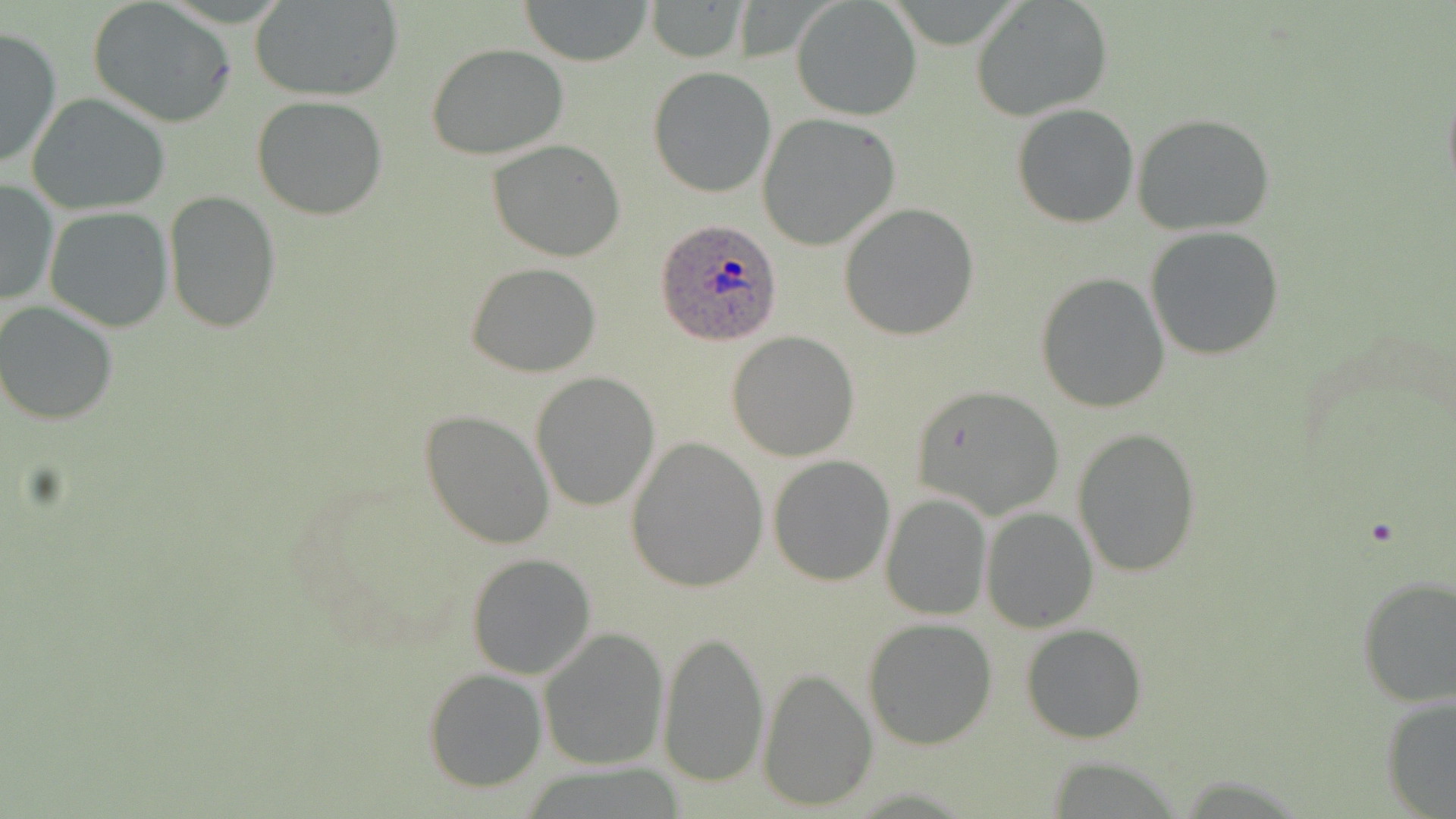
Approximate bounding boxes as named x1/y1/x2/y2 corners in pixels. Uninfected red blood cell locations: (x1=518, y1=0, x2=656, y2=66), (x1=250, y1=1, x2=404, y2=101), (x1=645, y1=1, x2=754, y2=64), (x1=794, y1=1, x2=921, y2=122), (x1=971, y1=2, x2=1113, y2=121), (x1=87, y1=4, x2=235, y2=127), (x1=0, y1=26, x2=62, y2=171), (x1=426, y1=44, x2=570, y2=162), (x1=648, y1=67, x2=777, y2=197), (x1=1441, y1=76, x2=1456, y2=201), (x1=27, y1=92, x2=171, y2=214), (x1=250, y1=96, x2=389, y2=221), (x1=1012, y1=103, x2=1140, y2=228), (x1=757, y1=113, x2=901, y2=250), (x1=1131, y1=113, x2=1275, y2=236), (x1=488, y1=139, x2=627, y2=261), (x1=1, y1=178, x2=58, y2=307), (x1=163, y1=190, x2=281, y2=333), (x1=838, y1=202, x2=981, y2=341), (x1=44, y1=206, x2=174, y2=332), (x1=1146, y1=226, x2=1284, y2=361), (x1=465, y1=261, x2=601, y2=378), (x1=1035, y1=272, x2=1171, y2=412), (x1=0, y1=302, x2=120, y2=424), (x1=726, y1=331, x2=859, y2=461), (x1=530, y1=371, x2=659, y2=511), (x1=908, y1=384, x2=1064, y2=520), (x1=420, y1=411, x2=554, y2=550), (x1=1073, y1=428, x2=1202, y2=579), (x1=626, y1=436, x2=769, y2=593), (x1=767, y1=455, x2=895, y2=587), (x1=880, y1=492, x2=992, y2=622), (x1=980, y1=506, x2=1096, y2=632), (x1=467, y1=552, x2=597, y2=680), (x1=1356, y1=576, x2=1455, y2=706), (x1=862, y1=618, x2=997, y2=749), (x1=1021, y1=624, x2=1148, y2=743), (x1=537, y1=626, x2=669, y2=772), (x1=659, y1=630, x2=769, y2=785), (x1=424, y1=667, x2=547, y2=792), (x1=758, y1=667, x2=876, y2=811), (x1=1381, y1=694, x2=1456, y2=818). Plasmodium ovale-infected red blood cell locations: (x1=654, y1=218, x2=782, y2=347). Slide-level diagnosis: Plasmodium ovale. Thin blood smear. Image is 1456×819 pixels. Single field of view. Light microscopy. May-Grünwald-Giemsa-stained preparation. Captured at 1000x magnification.